Locate every blood parasite and identify its species.
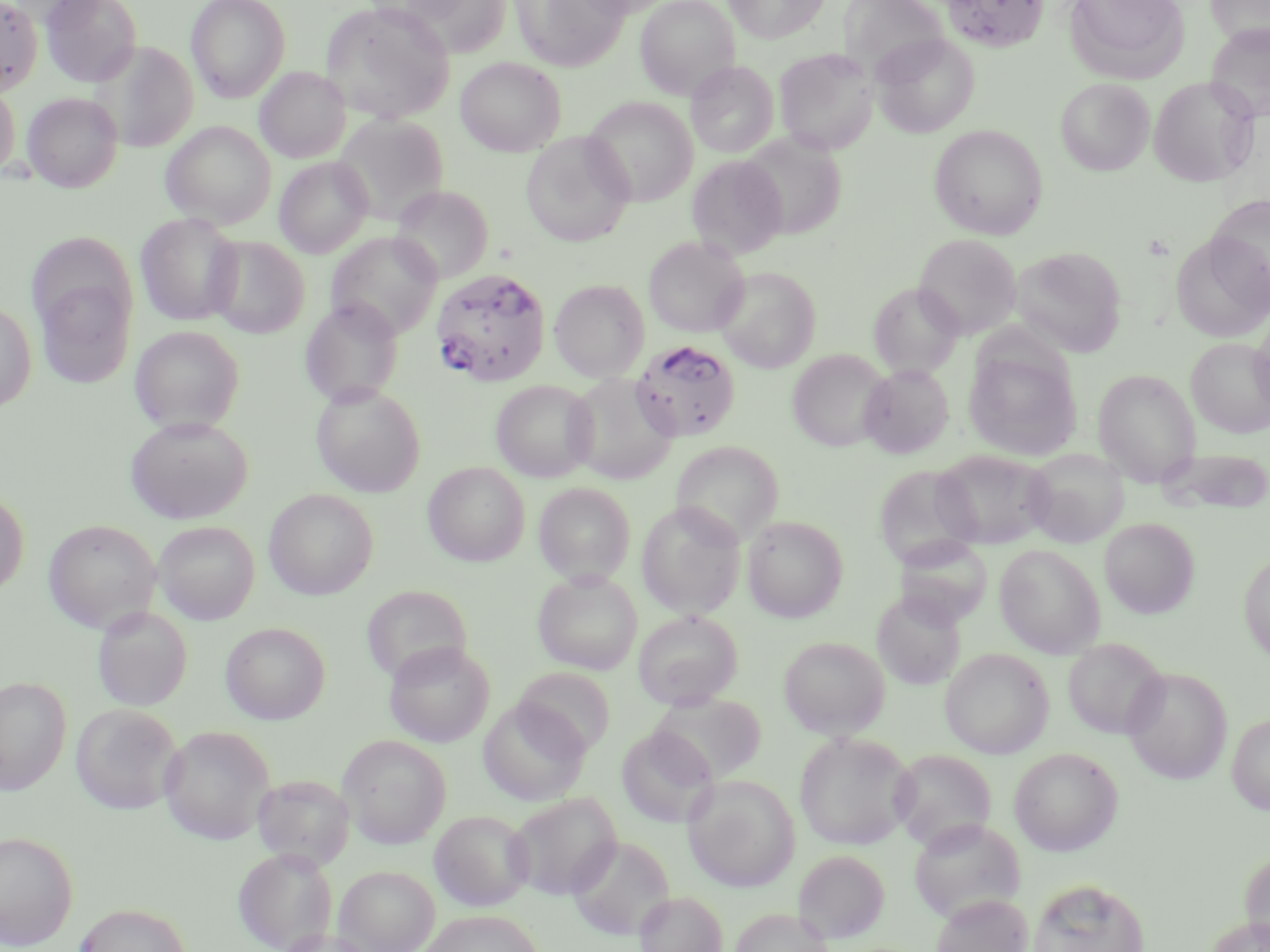

Approximate bounding boxes as [x1, y1, x2, y2] in pixels.
Plasmodium falciparum-infected red blood cells: [432, 268, 551, 386], [631, 339, 740, 442].
No Plasmodium ovale, Plasmodium malariae, Plasmodium vivax, Babesia divergens, or Trypanosoma brucei observed.

Uninfected red blood cell locations: [0, 0, 43, 95], [40, 0, 141, 87], [186, 0, 290, 101], [511, 0, 629, 70], [575, 0, 674, 17], [635, 0, 740, 100], [724, 0, 829, 43], [942, 0, 1048, 51], [1065, 0, 1189, 84], [1206, 0, 1270, 48], [403, 1, 512, 56], [320, 2, 455, 123], [839, 2, 950, 88], [1206, 24, 1270, 124], [872, 33, 980, 138], [91, 41, 199, 152], [773, 47, 879, 155], [456, 57, 565, 156], [687, 61, 779, 158], [255, 67, 350, 163], [1148, 76, 1259, 186], [1055, 78, 1154, 176], [0, 83, 20, 179], [23, 92, 123, 192], [583, 97, 698, 206], [332, 115, 450, 225], [161, 121, 277, 228], [929, 124, 1048, 239], [522, 132, 635, 247], [739, 132, 847, 239], [687, 155, 788, 259], [274, 156, 374, 258], [389, 185, 492, 285], [1206, 195, 1270, 307], [135, 213, 243, 325], [1170, 229, 1269, 341], [326, 232, 443, 339], [914, 234, 1021, 338], [206, 236, 310, 339], [643, 236, 749, 337], [1011, 247, 1127, 357], [715, 266, 821, 372], [34, 271, 136, 390], [549, 279, 650, 382], [868, 282, 964, 378], [300, 298, 404, 407], [0, 301, 36, 413], [1250, 314, 1270, 419], [130, 326, 244, 433], [1186, 337, 1269, 437], [787, 349, 892, 451], [965, 349, 1081, 461], [859, 364, 953, 459], [1093, 368, 1201, 484], [565, 373, 678, 484], [491, 380, 598, 482], [310, 383, 426, 497], [125, 415, 252, 524], [671, 440, 785, 546], [1160, 447, 1270, 514], [1023, 448, 1129, 548], [932, 450, 1053, 549], [423, 462, 530, 566], [874, 464, 983, 568], [533, 482, 636, 585], [0, 488, 28, 597], [263, 489, 378, 599], [637, 500, 746, 618], [742, 515, 848, 622], [1100, 517, 1199, 618], [43, 519, 161, 633], [154, 521, 259, 624], [894, 536, 994, 627], [995, 545, 1105, 658], [1239, 550, 1270, 665], [533, 571, 642, 674], [361, 585, 473, 684], [872, 590, 966, 689], [92, 606, 192, 712], [633, 610, 743, 709], [221, 622, 330, 724], [779, 636, 890, 739], [1063, 638, 1167, 739], [384, 640, 495, 747], [940, 648, 1053, 758], [1121, 666, 1233, 785], [514, 667, 616, 756], [0, 675, 71, 795], [650, 693, 766, 783], [480, 698, 590, 807], [71, 704, 182, 814], [1227, 712, 1270, 814], [159, 725, 275, 845], [617, 726, 718, 828], [794, 731, 915, 851], [338, 735, 451, 847], [1009, 747, 1123, 856], [890, 749, 996, 851], [683, 774, 800, 892], [251, 775, 355, 871], [507, 792, 622, 900], [430, 810, 534, 911], [908, 817, 1025, 924], [0, 830, 78, 950], [567, 835, 675, 941], [233, 846, 338, 952], [1240, 849, 1270, 951], [794, 850, 890, 943], [334, 865, 440, 952], [1027, 877, 1150, 952], [635, 891, 727, 952], [930, 893, 1032, 952], [74, 902, 190, 952], [730, 908, 835, 952], [420, 910, 543, 952], [1204, 915, 1270, 952], [276, 928, 381, 952]. Slide-level diagnosis: Plasmodium falciparum. Single field of view. 1000x magnification. Image is 1270×952 pixels. Thin blood film. May-Grünwald-Giemsa stain. Optical microscopy.